Locate every Plasmodium ovale-infected red blood cell.
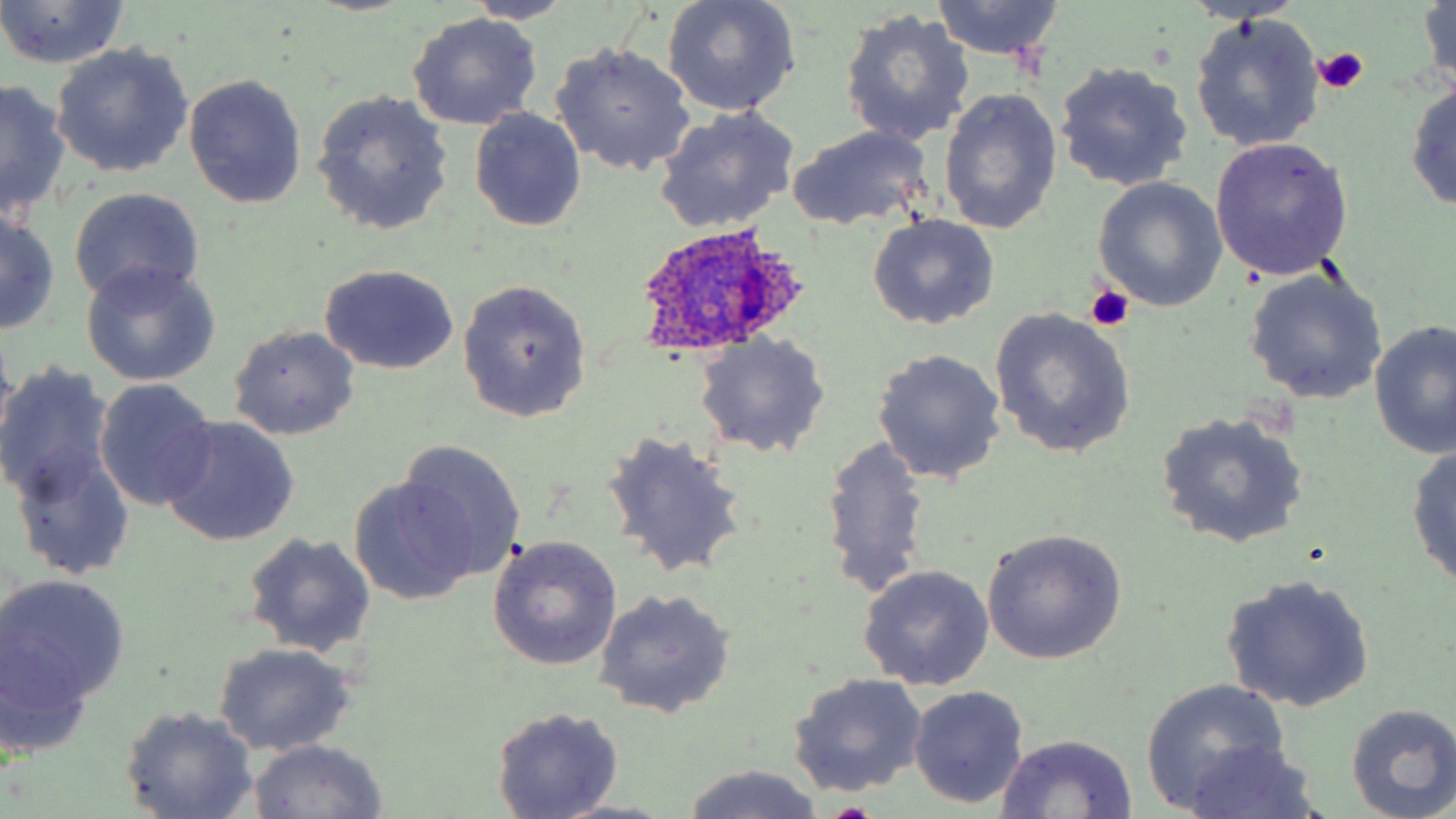
Approximate bounding boxes as named x1/y1/x2/y2 corners in pixels.
Plasmodium ovale-infected red blood cells: (x1=628, y1=224, x2=813, y2=357).

Summary:
  - Uninfected red blood cell locations: (x1=465, y1=0, x2=579, y2=24), (x1=661, y1=0, x2=802, y2=116), (x1=1418, y1=0, x2=1454, y2=95), (x1=929, y1=1, x2=1065, y2=60), (x1=0, y1=2, x2=130, y2=69), (x1=839, y1=7, x2=975, y2=148), (x1=407, y1=12, x2=543, y2=131), (x1=1189, y1=14, x2=1325, y2=153), (x1=551, y1=43, x2=695, y2=176), (x1=49, y1=44, x2=193, y2=179), (x1=1054, y1=61, x2=1194, y2=194), (x1=183, y1=73, x2=307, y2=209), (x1=1405, y1=76, x2=1456, y2=215), (x1=1, y1=80, x2=70, y2=223), (x1=311, y1=89, x2=454, y2=237), (x1=940, y1=89, x2=1062, y2=235), (x1=655, y1=105, x2=802, y2=232), (x1=469, y1=107, x2=587, y2=232), (x1=787, y1=126, x2=933, y2=231), (x1=1209, y1=135, x2=1354, y2=279), (x1=1092, y1=178, x2=1227, y2=311), (x1=68, y1=187, x2=206, y2=306), (x1=0, y1=210, x2=60, y2=335), (x1=867, y1=214, x2=1000, y2=330), (x1=81, y1=263, x2=220, y2=386), (x1=320, y1=265, x2=459, y2=376), (x1=1242, y1=266, x2=1387, y2=406), (x1=456, y1=280, x2=592, y2=422), (x1=988, y1=306, x2=1137, y2=457), (x1=1370, y1=319, x2=1456, y2=460), (x1=229, y1=325, x2=361, y2=440), (x1=694, y1=332, x2=830, y2=458), (x1=871, y1=348, x2=1007, y2=484), (x1=0, y1=368, x2=115, y2=507), (x1=93, y1=379, x2=219, y2=512), (x1=1155, y1=412, x2=1310, y2=550), (x1=157, y1=417, x2=300, y2=547), (x1=601, y1=430, x2=749, y2=581), (x1=819, y1=436, x2=932, y2=600), (x1=395, y1=439, x2=528, y2=581), (x1=1406, y1=442, x2=1456, y2=593), (x1=12, y1=444, x2=135, y2=580), (x1=348, y1=479, x2=475, y2=602), (x1=983, y1=528, x2=1127, y2=666), (x1=242, y1=533, x2=376, y2=657), (x1=488, y1=535, x2=623, y2=671), (x1=857, y1=564, x2=994, y2=690), (x1=1220, y1=573, x2=1376, y2=712), (x1=0, y1=574, x2=130, y2=712), (x1=593, y1=589, x2=735, y2=718), (x1=211, y1=641, x2=359, y2=756), (x1=787, y1=673, x2=927, y2=798), (x1=1141, y1=679, x2=1291, y2=811), (x1=908, y1=686, x2=1030, y2=810), (x1=1346, y1=704, x2=1456, y2=818), (x1=120, y1=706, x2=259, y2=818), (x1=491, y1=706, x2=624, y2=818), (x1=995, y1=733, x2=1138, y2=817), (x1=246, y1=740, x2=391, y2=819), (x1=1178, y1=740, x2=1324, y2=818), (x1=676, y1=763, x2=834, y2=819), (x1=552, y1=799, x2=678, y2=819)
  - Platelet locations: (x1=1313, y1=48, x2=1368, y2=93), (x1=1086, y1=285, x2=1133, y2=331)
  - Slide-level diagnosis: Plasmodium ovale
  - Magnification: 1000x
  - Field of view: single
  - Preparation: thin blood film
  - Stain: May-Grünwald-Giemsa
  - Image size: 1456×819 pixels
  - Modality: light microscopy